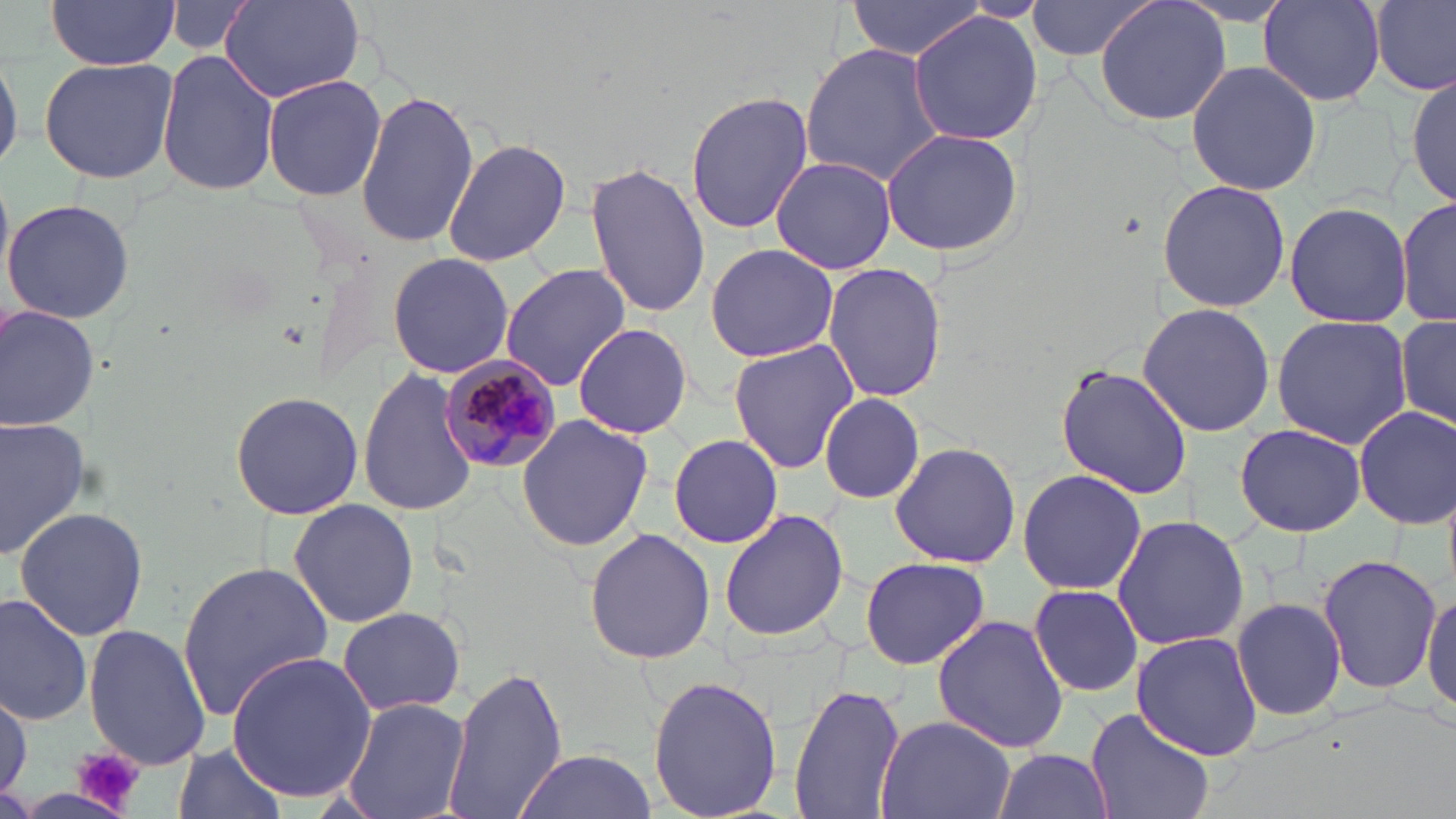

Summary:
  - Coordinate format: approximate bounding boxes as named x1/y1/x2/y2 corners in pixels
  - Uninfected red blood cell locations: (x1=47, y1=0, x2=180, y2=69), (x1=221, y1=0, x2=365, y2=103), (x1=845, y1=0, x2=992, y2=60), (x1=1025, y1=0, x2=1163, y2=62), (x1=1095, y1=0, x2=1232, y2=127), (x1=1370, y1=0, x2=1456, y2=95), (x1=166, y1=2, x2=256, y2=57), (x1=1258, y1=2, x2=1386, y2=107), (x1=909, y1=11, x2=1044, y2=147), (x1=0, y1=42, x2=20, y2=179), (x1=801, y1=43, x2=948, y2=186), (x1=157, y1=50, x2=278, y2=197), (x1=37, y1=56, x2=179, y2=185), (x1=1187, y1=60, x2=1322, y2=194), (x1=1407, y1=68, x2=1455, y2=206), (x1=261, y1=73, x2=388, y2=202), (x1=357, y1=90, x2=478, y2=248), (x1=685, y1=92, x2=815, y2=235), (x1=880, y1=126, x2=1026, y2=257), (x1=442, y1=136, x2=572, y2=267), (x1=771, y1=155, x2=895, y2=274), (x1=586, y1=163, x2=710, y2=317), (x1=1157, y1=178, x2=1291, y2=313), (x1=1397, y1=196, x2=1456, y2=327), (x1=2, y1=197, x2=134, y2=323), (x1=1283, y1=201, x2=1414, y2=329), (x1=705, y1=244, x2=840, y2=362), (x1=386, y1=251, x2=515, y2=379), (x1=821, y1=263, x2=948, y2=402), (x1=498, y1=264, x2=629, y2=393), (x1=1137, y1=303, x2=1278, y2=435), (x1=0, y1=304, x2=100, y2=431), (x1=1270, y1=315, x2=1413, y2=448), (x1=1397, y1=316, x2=1456, y2=427), (x1=571, y1=322, x2=693, y2=438), (x1=726, y1=340, x2=859, y2=473), (x1=357, y1=362, x2=481, y2=519), (x1=1056, y1=363, x2=1193, y2=501), (x1=229, y1=390, x2=366, y2=520), (x1=816, y1=395, x2=927, y2=503), (x1=1354, y1=405, x2=1456, y2=530), (x1=517, y1=413, x2=655, y2=552), (x1=1, y1=416, x2=91, y2=561), (x1=1234, y1=423, x2=1367, y2=536), (x1=668, y1=434, x2=783, y2=547), (x1=887, y1=442, x2=1022, y2=570), (x1=1018, y1=469, x2=1147, y2=594), (x1=288, y1=500, x2=419, y2=629), (x1=13, y1=504, x2=149, y2=644), (x1=716, y1=507, x2=850, y2=647), (x1=1110, y1=515, x2=1249, y2=651), (x1=584, y1=529, x2=716, y2=666), (x1=1315, y1=553, x2=1441, y2=693), (x1=858, y1=556, x2=991, y2=671), (x1=178, y1=558, x2=334, y2=725), (x1=1029, y1=583, x2=1142, y2=697), (x1=1423, y1=585, x2=1456, y2=719), (x1=0, y1=591, x2=93, y2=726), (x1=1232, y1=596, x2=1348, y2=721), (x1=337, y1=606, x2=466, y2=715), (x1=932, y1=614, x2=1069, y2=755), (x1=83, y1=625, x2=214, y2=770), (x1=1130, y1=631, x2=1263, y2=760), (x1=224, y1=650, x2=376, y2=804), (x1=440, y1=664, x2=569, y2=819), (x1=648, y1=676, x2=783, y2=819), (x1=787, y1=684, x2=908, y2=819), (x1=0, y1=687, x2=30, y2=803), (x1=339, y1=696, x2=471, y2=819), (x1=1085, y1=707, x2=1216, y2=819), (x1=872, y1=716, x2=1019, y2=819), (x1=172, y1=741, x2=288, y2=819), (x1=992, y1=747, x2=1112, y2=819), (x1=510, y1=749, x2=659, y2=819)
  - Plasmodium malariae-infected red blood cell locations: (x1=437, y1=358, x2=561, y2=477)
  - Platelet locations: (x1=74, y1=748, x2=145, y2=812)
  - Slide-level diagnosis: Plasmodium malariae
  - Modality: light microscopy
  - Stain: May-Grünwald-Giemsa
  - Field of view: one of a larger specimen
  - Image size: 1456×819 pixels
  - Magnification: 1000x
  - Preparation: thin blood film